Classify this cell by malaria status.
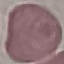

It is uninfected.

{
  "capture": "smartphone camera at the microscope eyepiece",
  "preparation": "thin smear",
  "image_type": "automatically extracted cell patch, resized to 64 × 64 pixels",
  "stain": "Giemsa"
}